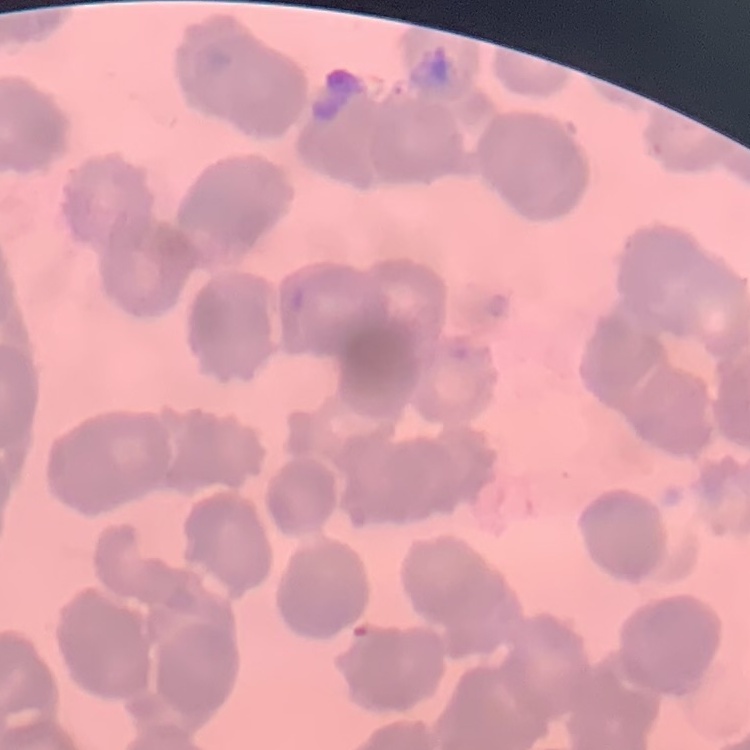
Summary:
  - Red blood cell morphology: rouleaux formation
  - Image type: square crop of a larger photomicrograph
  - Preparation: thin blood smear
  - Stain: Field's or Giemsa